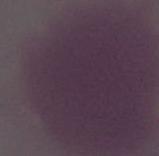
Summary:
  - Modality: micrograph
  - Identification: red blood cell
  - Magnification: 1000x